Classify this cell by malaria status.
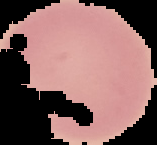

Uninfected.

Summary:
  - Image size: 157×145 pixels
  - Preparation: thin blood smear
  - Image type: segmented cell region with the area outside set to black